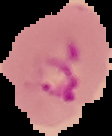 Result: malaria parasites detected. From a thin blood smear. Image is 112×136 pixels. Cell region segmented out of the field of view; the surrounding area is masked to black.